Report the malaria status of this cell.
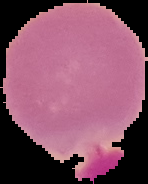
Uninfected.

The area outside the segmented cell region is set to black. From a thin blood smear. Image is 148×184 pixels.